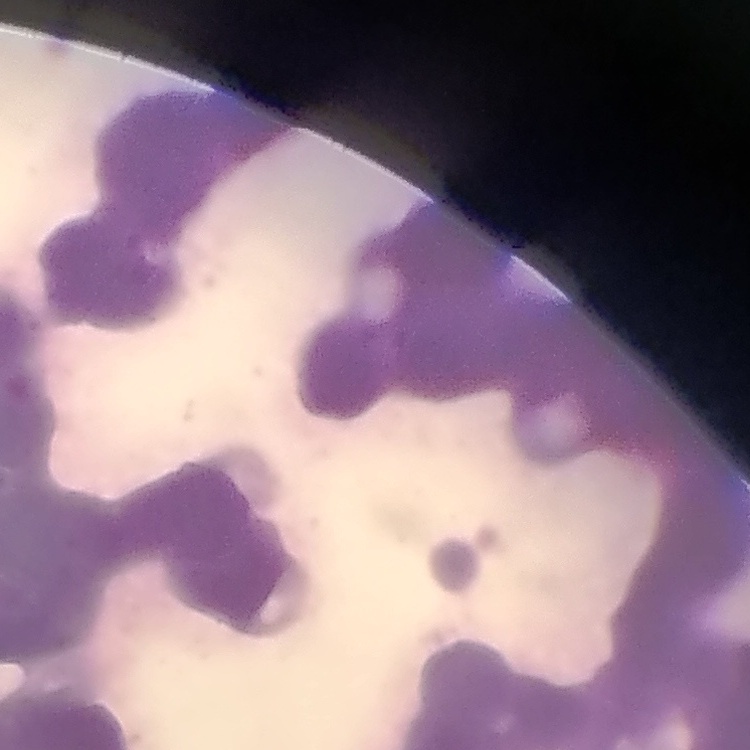
Summary:
  - Red blood cell morphology: rouleaux formation
  - Stain: Field's or Giemsa
  - Image type: one tile cut from a larger photomicrograph
  - Preparation: thin blood film